Assess this cell for malaria.
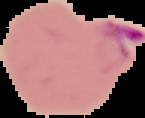

Parasitized.

Summary:
  - Image type: segmented cell region with the area outside set to black
  - Preparation: thin blood film
  - Image size: 145×118 pixels